Report the malaria status of this cell.
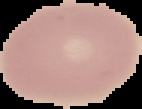
It is uninfected.

image size = 142×109 pixels
preparation = thin blood film
image type = segmented cell region with the area outside set to black